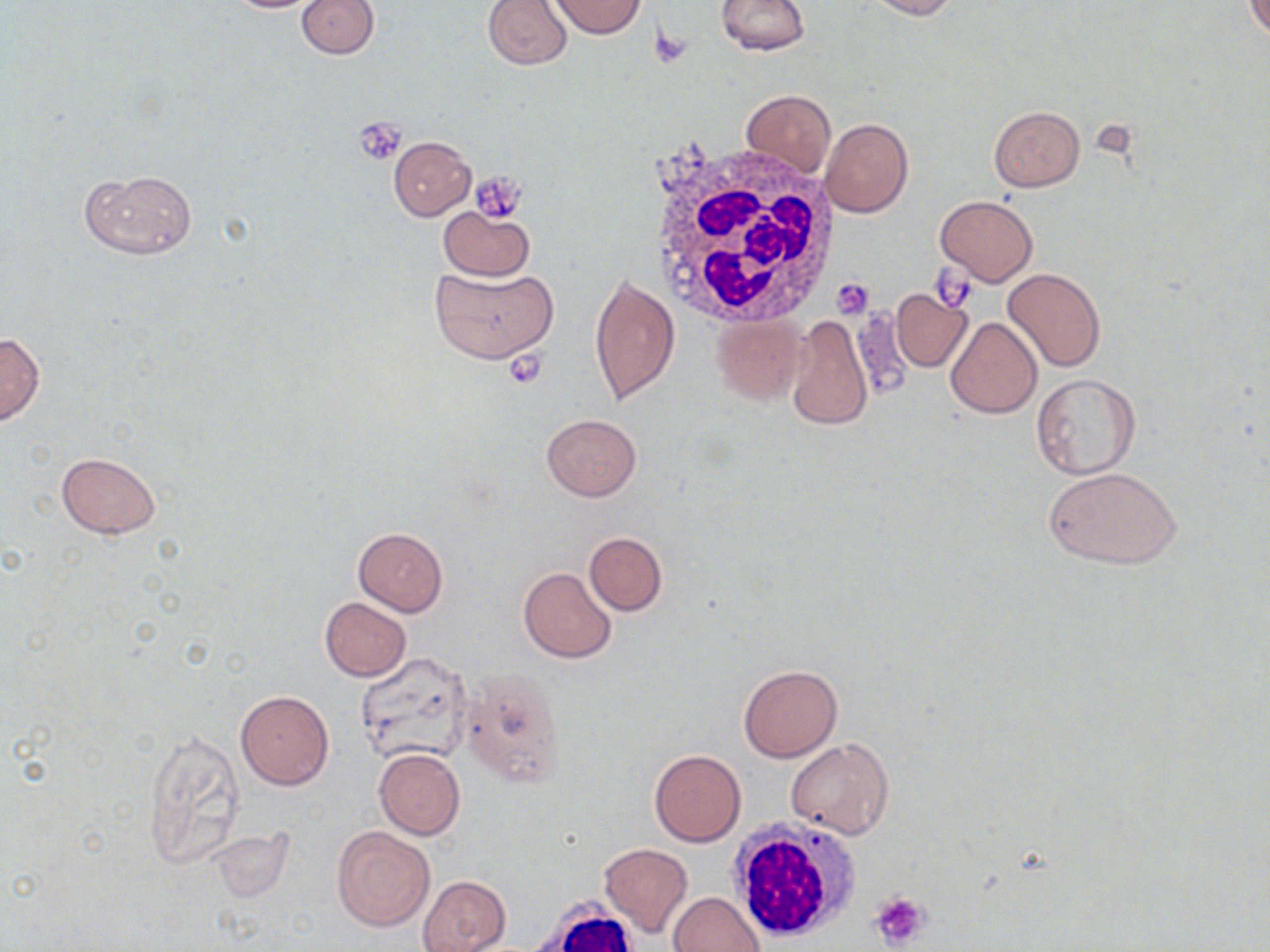

slide-level diagnosis = negative for blood parasites
image size = 1270×952 pixels
white blood cell locations = approximate bounding boxes as (x1, y1, x2, y2) in pixels: (640, 137, 841, 327), (725, 821, 861, 943), (536, 902, 639, 952)
magnification = 1000x
preparation = thin blood film
field of view = single
platelet locations = approximate bounding boxes as (x1, y1, x2, y2) in pixels: (649, 28, 692, 69), (354, 118, 408, 165), (471, 172, 525, 224), (932, 264, 975, 311), (832, 277, 874, 318), (503, 349, 551, 388), (868, 891, 930, 948)
stain = May-Grünwald-Giemsa
uninfected red blood cell locations = approximate bounding boxes as (x1, y1, x2, y2) in pixels: (222, 0, 330, 14), (297, 0, 380, 58), (481, 0, 573, 70), (549, 0, 647, 39), (716, 0, 811, 55), (864, 0, 959, 19), (1247, 1, 1270, 40), (740, 88, 836, 179), (987, 106, 1085, 191), (819, 116, 913, 218), (388, 136, 476, 220), (79, 169, 197, 259), (935, 195, 1037, 286), (437, 205, 535, 280), (429, 265, 559, 363), (1003, 268, 1106, 374), (588, 273, 680, 409), (890, 288, 973, 373), (849, 306, 913, 404), (785, 314, 873, 433), (710, 315, 807, 405), (945, 317, 1041, 419), (0, 332, 45, 426), (1030, 373, 1142, 478), (542, 413, 641, 500), (56, 453, 162, 539), (1043, 464, 1182, 571), (353, 527, 447, 616), (584, 532, 667, 616), (518, 566, 617, 663), (319, 597, 411, 681), (355, 651, 476, 765), (737, 664, 842, 761), (461, 670, 565, 789), (235, 690, 333, 790), (141, 730, 246, 869), (787, 737, 894, 840), (374, 747, 466, 840), (648, 748, 746, 847), (332, 825, 434, 931), (204, 828, 294, 903), (598, 844, 693, 938), (419, 875, 511, 952), (669, 891, 765, 952)
modality = optical microscopy